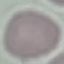
Result: negative for malaria parasites. Giemsa stain. Automatically extracted cell patch, resized to 64 × 64 pixels. Photographed with a smartphone camera at the microscope eyepiece. Thin blood film.